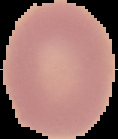
Segmented cell region on a black background. From a thin blood film. Image is 118×139 pixels. Result: negative for malaria parasites.